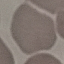

Summary:
  - Result: no malaria parasites seen
  - Capture: smartphone camera at the microscope eyepiece
  - Image type: cell patch, automatically extracted from a larger field of view and resized to 64 × 64 pixels
  - Preparation: thin blood smear
  - Stain: Giemsa